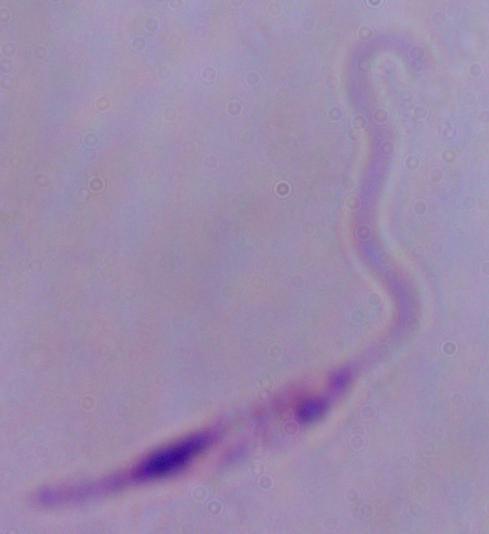

{
  "identification": "Leishmania",
  "modality": "micrograph",
  "magnification": "1000x"
}